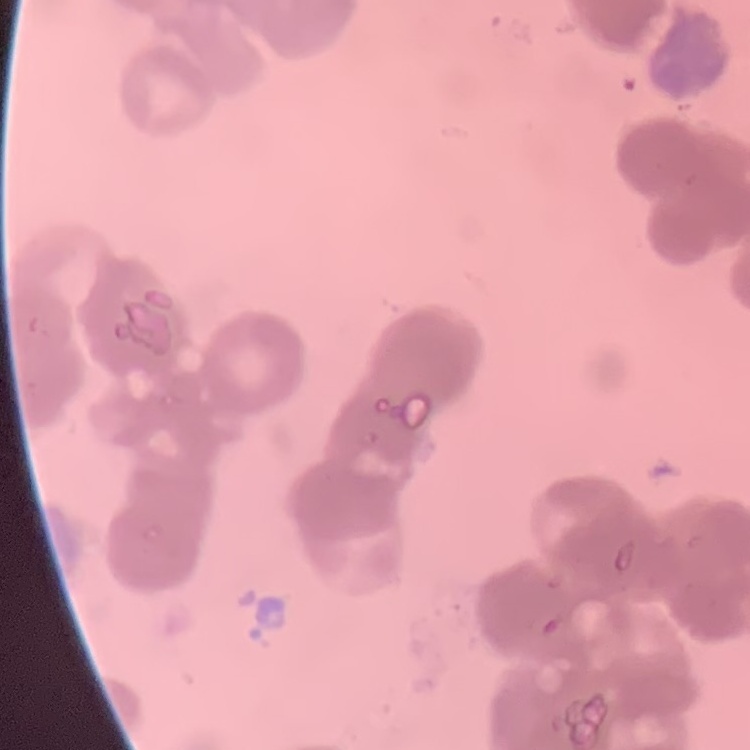

erythrocyte morphology = rouleaux formation
preparation = thin peripheral smear
stain = Field's or Giemsa
image type = square crop of a larger photomicrograph